Assess this cell for malaria.
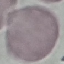
Uninfected.

Summary:
  - Stain: Giemsa
  - Preparation: thin blood smear
  - Image type: automatically extracted cell patch, resized to 64 × 64 pixels
  - Capture: smartphone through the microscope eyepiece